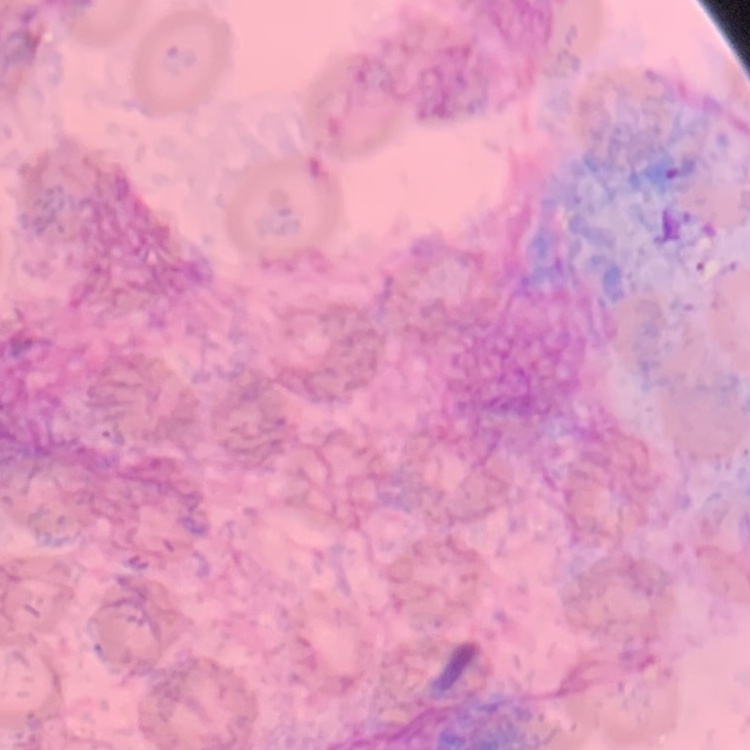
erythrocyte morphology = no rouleaux formation
stain = Field's or Giemsa
image type = square crop of a larger photomicrograph
preparation = thin blood smear